Assess this cell for malaria.
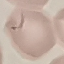
It is uninfected.

Thin smear of blood. Cell patch, automatically extracted from a larger field of view and resized to 64 × 64 pixels. Photographed with a smartphone camera at the microscope eyepiece. Giemsa stain.